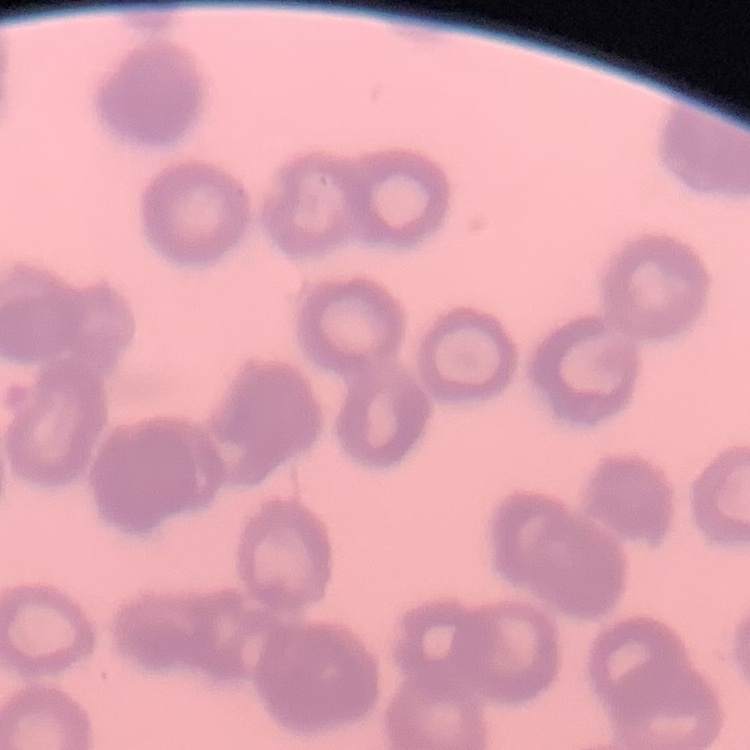
erythrocyte morphology = rouleaux formation
stain = Field's or Giemsa
image type = square crop of a larger photomicrograph
preparation = thin blood smear